State which parasite is depicted.
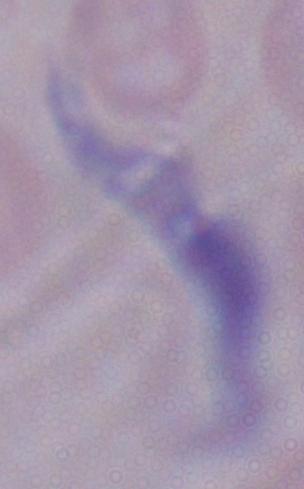
A trypanosome.

Summary:
  - Magnification: 1000x
  - Modality: photomicrograph